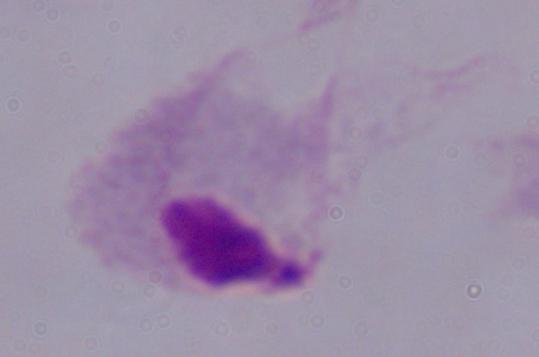
magnification = 1000x
modality = photomicrograph
identification = trichomonad